Give the position of every P. falciparum parasite, noting its life-cycle stage.
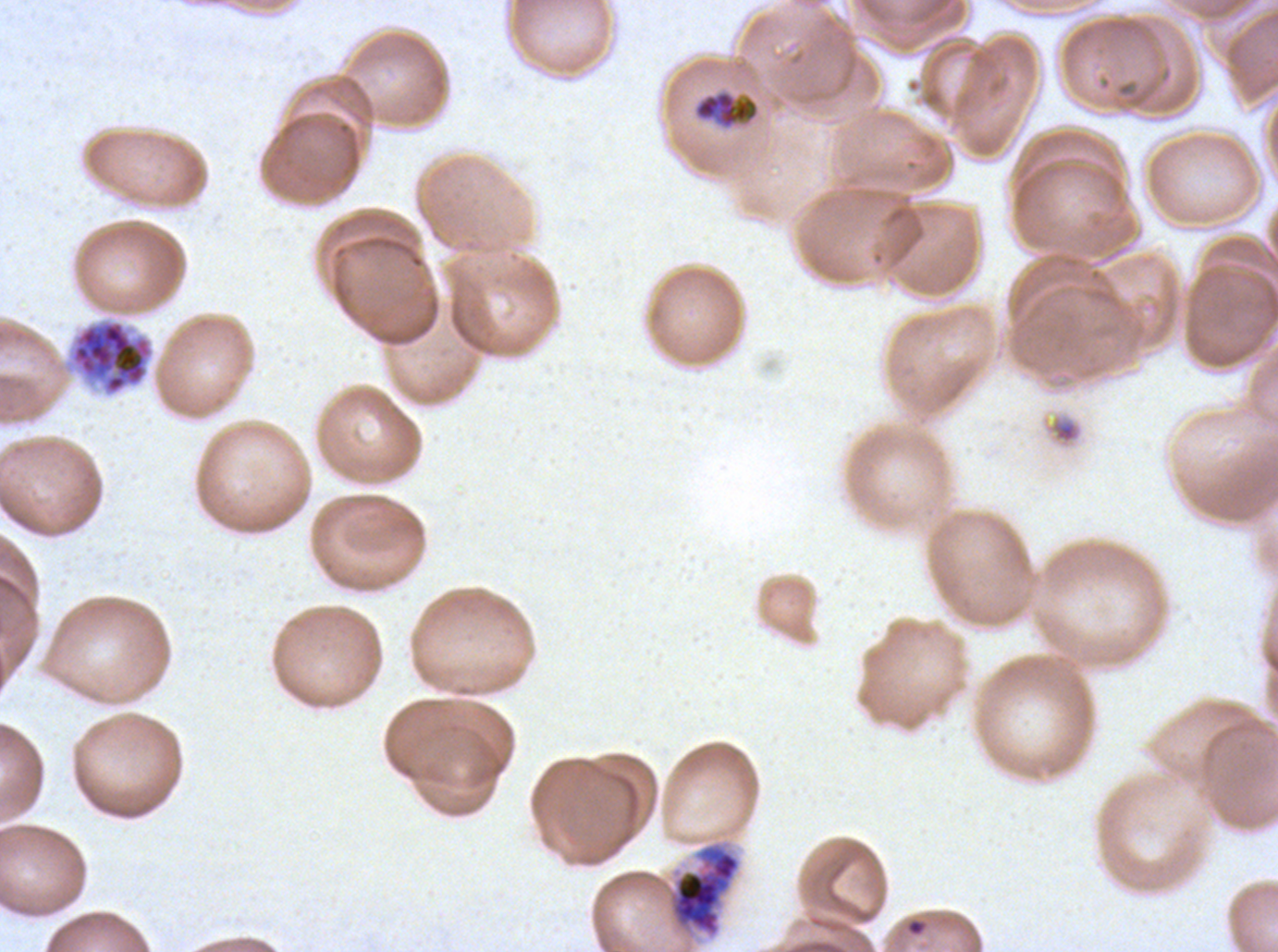
Approximate bounding boxes as (x1, y1, x2, y2) in pixels.
Late trophozoites: (694, 91, 759, 128).
Early schizonts: (667, 841, 742, 938).
Segmenters: (61, 317, 155, 398).
No rings, late-ring/early-trophozoite forms, mid trophozoites, late schizonts, or gametocytes observed.

Summary:
  - Debris locations: (1049, 415, 1082, 445)
  - Image size: 1278×952 pixels
  - Life-cycle stages observed: late trophozoite, early schizont, segmenter
  - Preparation: thin blood smear
  - Field of view: one sub-image of a larger composite
  - Specimen: P. falciparum from a patient in The Gambia, cultured ex vivo for 24 to 48 hours
  - Stain: Giemsa